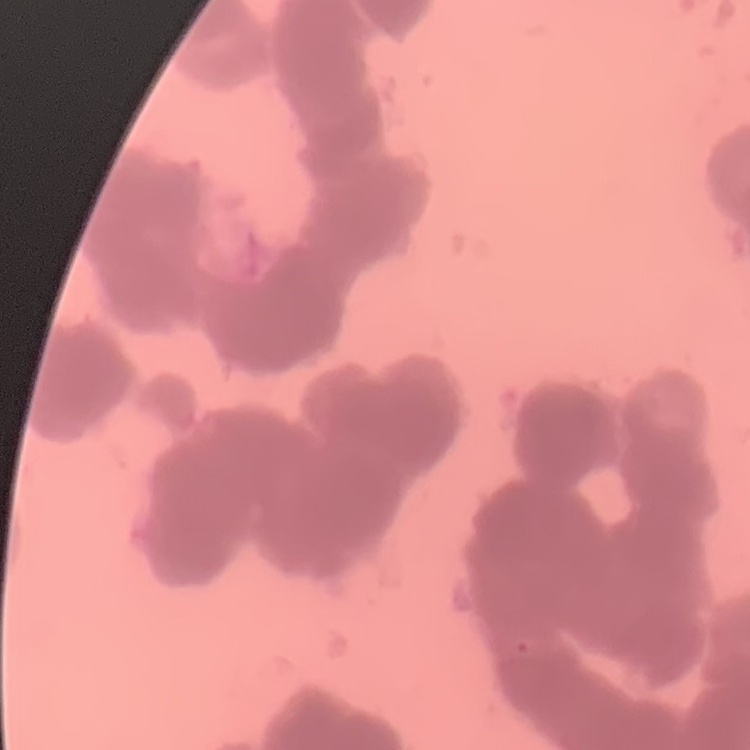

Summary:
  - Erythrocyte morphology: rouleaux formation
  - Image type: one tile cut from a larger photomicrograph
  - Preparation: thin peripheral smear
  - Stain: Field's or Giemsa